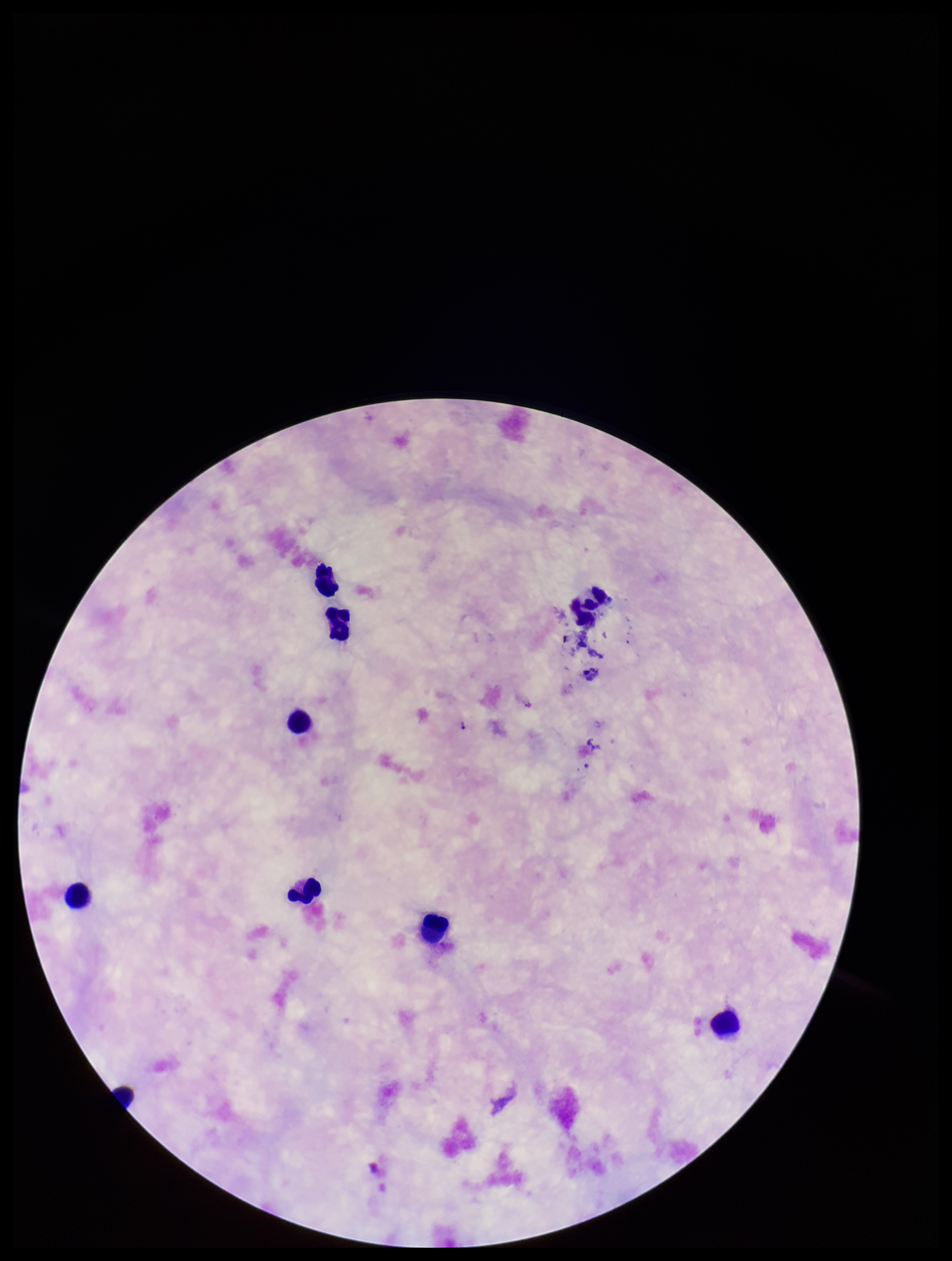
Preparation: thick smear. Parasite count: 0. Patient malaria status: negative. Image is 952×1261 pixels. Leukocyte count: 9. Plasmodium parasites: none detected. Single field of view. Giemsa stain. Smartphone photograph taken through the eyepiece of a microscope.